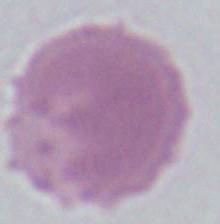
Captured at 1000x magnification. A red blood cell is shown. Micrograph.